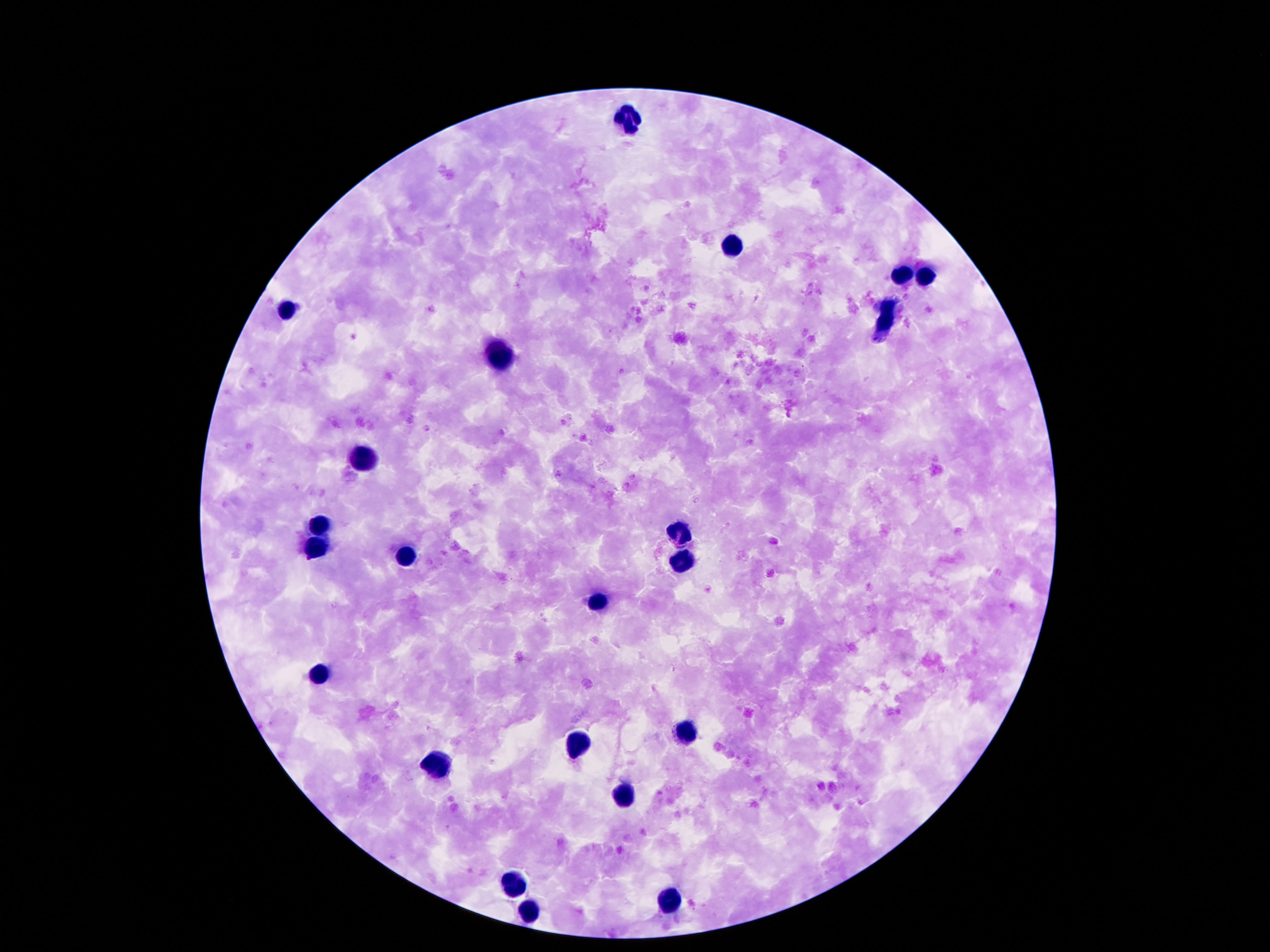 Approximate object centers, in pixels from the top-left corner. Leukocyte locations: (x=630, y=120), (x=732, y=251), (x=900, y=274), (x=925, y=274), (x=290, y=313), (x=886, y=324), (x=501, y=354), (x=364, y=461), (x=319, y=526), (x=677, y=532), (x=315, y=546), (x=405, y=555), (x=683, y=561), (x=601, y=601), (x=317, y=673), (x=687, y=735), (x=575, y=743), (x=435, y=769), (x=622, y=796), (x=517, y=880), (x=667, y=904), (x=528, y=912). Image is 1270×952 pixels. Giemsa stain. Patient malaria status: uninfected. Thick peripheral-blood smear. 100x magnification. Photographed through the microscope eyepiece with a smartphone camera. One field from this slide.